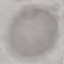

Malaria status: uninfected. Cell patch, automatically extracted from a larger field of view and resized to 64 × 64 pixels. Giemsa-stained preparation. Photographed with a smartphone camera at the microscope eyepiece. Thin smear of blood.